Report the malaria status of this cell.
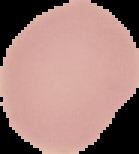
It is uninfected.

{
  "image_size": "139×154 pixels",
  "image_type": "cell region segmented out of the field of view; surrounding area masked to black",
  "preparation": "thin blood film"
}